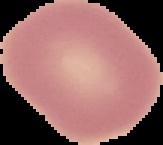

{
  "preparation": "thin blood film",
  "image_type": "segmented cell region with the area outside set to black",
  "malaria_status": "uninfected",
  "image_size": "163×145 pixels"
}